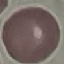

Result: no malaria parasites seen. Thin blood film. Cell patch, automatically extracted from a larger field of view and resized to 64 × 64 pixels. Photographed with a smartphone camera at the microscope eyepiece. Giemsa-stained preparation.